Mark where platelets are.
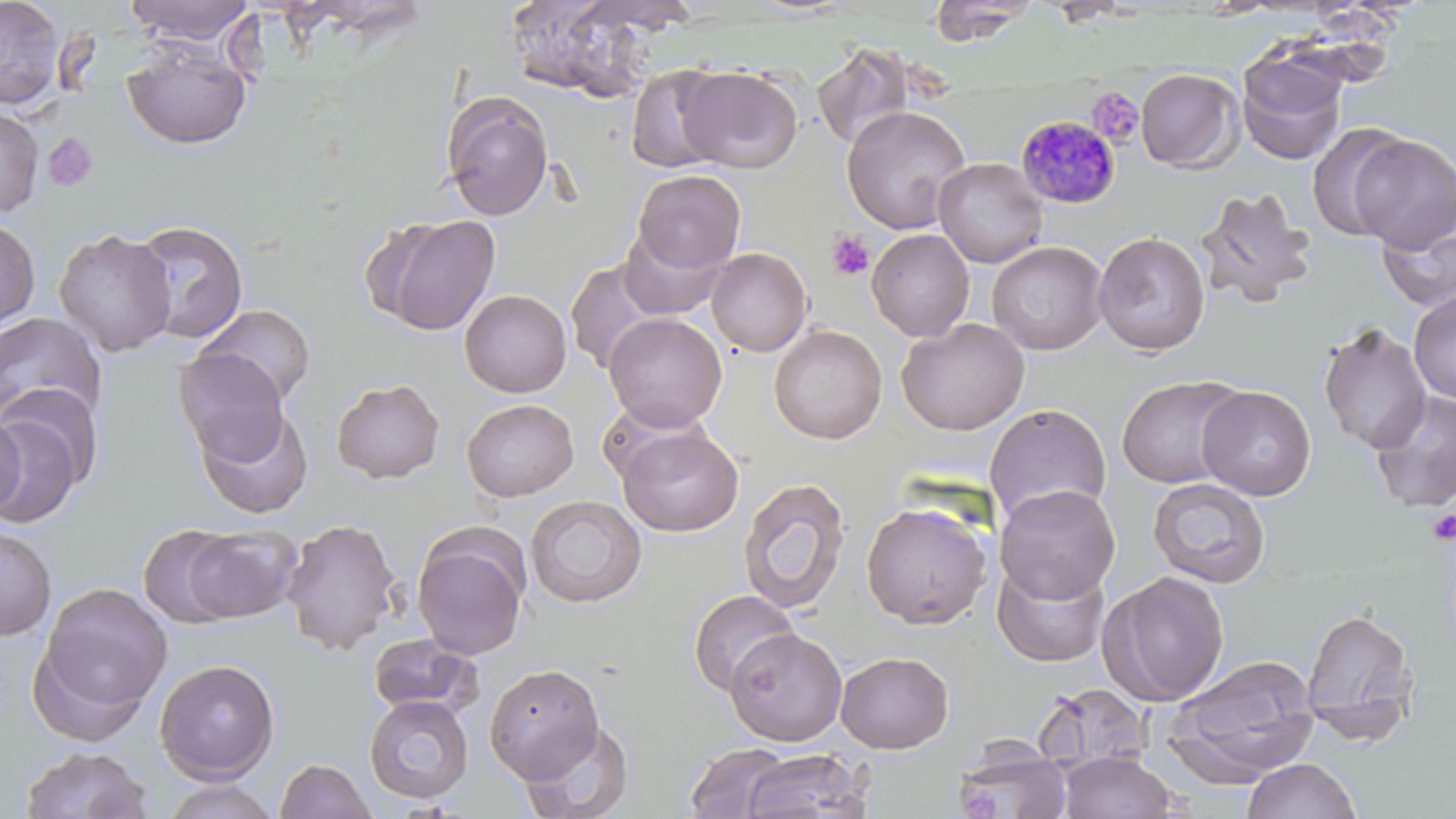

Approximate bounding boxes as [x1, y1, x2, y2] in pixels.
Platelets: [1087, 87, 1143, 146], [43, 132, 99, 192], [826, 230, 875, 281], [1427, 509, 1456, 544], [955, 782, 1002, 818].

Summary:
  - Uninfected red blood cell locations: [0, 0, 65, 109], [124, 0, 254, 46], [928, 0, 1038, 47], [502, 1, 659, 101], [122, 41, 252, 150], [812, 43, 917, 152], [1236, 50, 1348, 165], [626, 64, 732, 174], [678, 66, 802, 173], [1135, 68, 1244, 173], [441, 91, 554, 220], [841, 105, 971, 234], [0, 106, 44, 217], [1307, 122, 1413, 243], [1350, 134, 1456, 253], [933, 157, 1048, 268], [632, 169, 746, 275], [1194, 186, 1317, 309], [1377, 204, 1456, 313], [369, 214, 501, 336], [0, 216, 41, 332], [131, 220, 249, 346], [618, 226, 729, 320], [53, 228, 177, 357], [866, 228, 975, 340], [1093, 231, 1211, 356], [986, 240, 1108, 355], [706, 247, 812, 356], [564, 259, 669, 374], [459, 290, 572, 397], [1409, 291, 1456, 403], [194, 304, 316, 407], [0, 312, 107, 431], [603, 313, 727, 431], [897, 318, 1030, 435], [1316, 322, 1431, 455], [769, 324, 887, 444], [173, 348, 289, 462], [1115, 374, 1248, 488], [331, 377, 445, 484], [1197, 385, 1316, 500], [1368, 390, 1456, 513], [462, 399, 579, 501], [984, 402, 1112, 525], [195, 406, 314, 519], [0, 408, 85, 528], [0, 409, 26, 517], [617, 425, 743, 537], [738, 477, 851, 613], [1147, 477, 1271, 588], [995, 483, 1120, 603], [525, 495, 647, 608], [860, 500, 994, 630], [280, 517, 401, 655], [0, 524, 57, 640], [138, 524, 245, 629], [178, 526, 303, 623], [412, 531, 529, 660], [991, 557, 1110, 668], [1100, 571, 1230, 706], [36, 582, 173, 723], [688, 589, 800, 697], [1300, 607, 1419, 742], [724, 627, 848, 746], [367, 633, 485, 719], [835, 651, 955, 754], [1166, 655, 1321, 787], [154, 658, 280, 783], [485, 662, 604, 784], [1032, 683, 1154, 774], [363, 695, 474, 803], [519, 720, 636, 819], [685, 742, 792, 819], [956, 743, 1073, 818], [19, 746, 152, 819], [741, 749, 872, 818], [1059, 752, 1179, 818], [1241, 758, 1362, 819], [275, 759, 377, 819], [158, 778, 281, 819]
  - Plasmodium malariae-infected red blood cell locations: [1016, 115, 1122, 209]
  - Slide-level diagnosis: Plasmodium malariae
  - Stain: May-Grünwald-Giemsa
  - Modality: optical microscopy
  - Magnification: 1000x
  - Image size: 1456×819 pixels
  - Preparation: thin blood film
  - Field of view: one of a larger specimen